Classify this cell by malaria status.
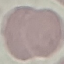

It is uninfected.

capture = smartphone camera at the microscope eyepiece
stain = Giemsa
image type = cell patch, automatically extracted from a larger field of view and resized to 64 × 64 pixels
preparation = thin smear